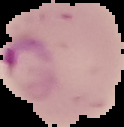

Malaria status: parasitized. Image is 124×127 pixels. The area outside the segmented cell region is set to black. From a thin blood smear.